Give the preparation type.
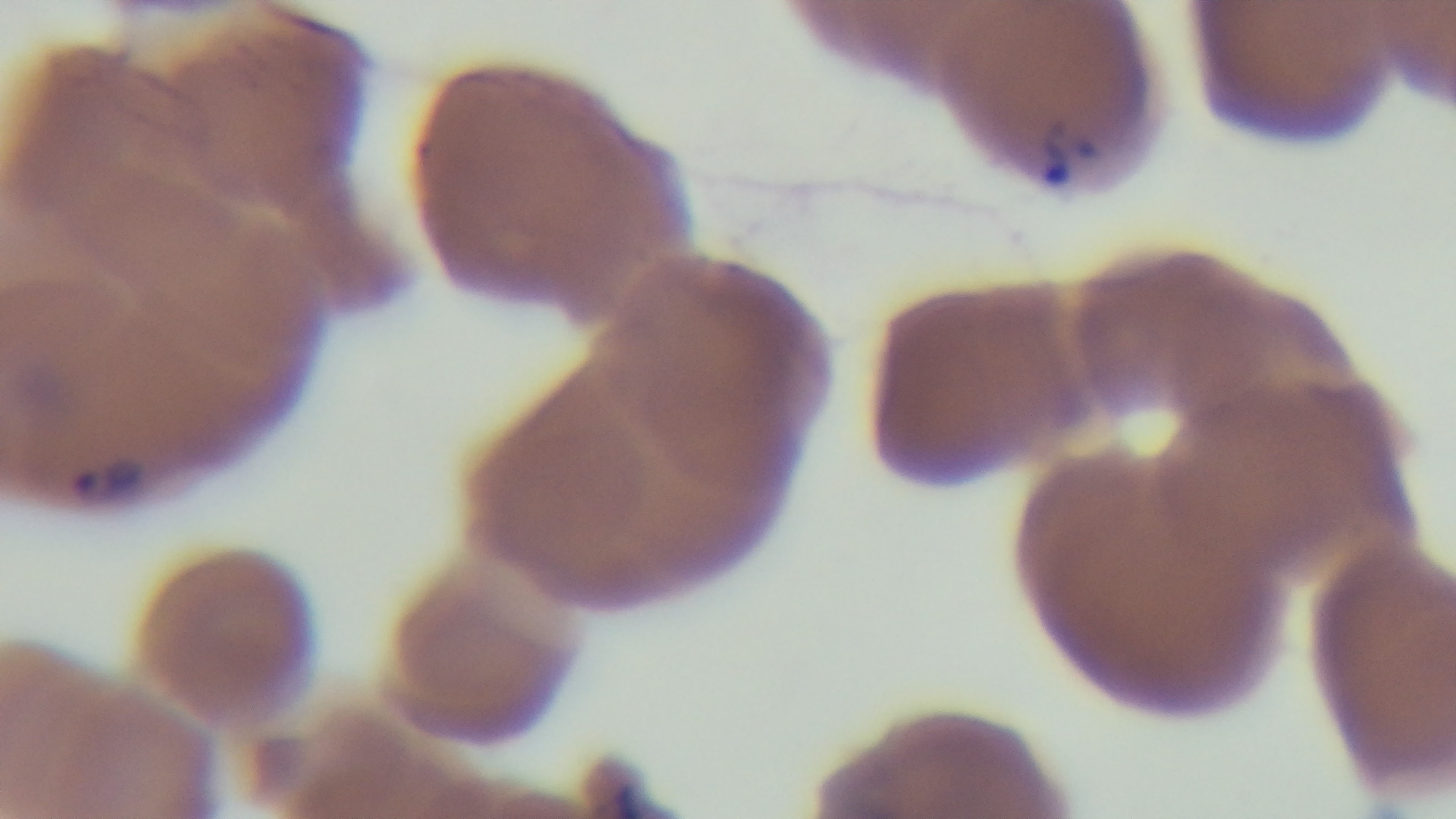
Thin.

Summary:
  - Malaria status: infected
  - Objective: 100x oil immersion
  - Field of view: one from the slide
  - Stain: Giemsa
  - Capture: mounted 4K digital camera
  - Modality: light microscopy